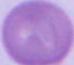 Micrograph. 1000x magnification. A red blood cell is shown.